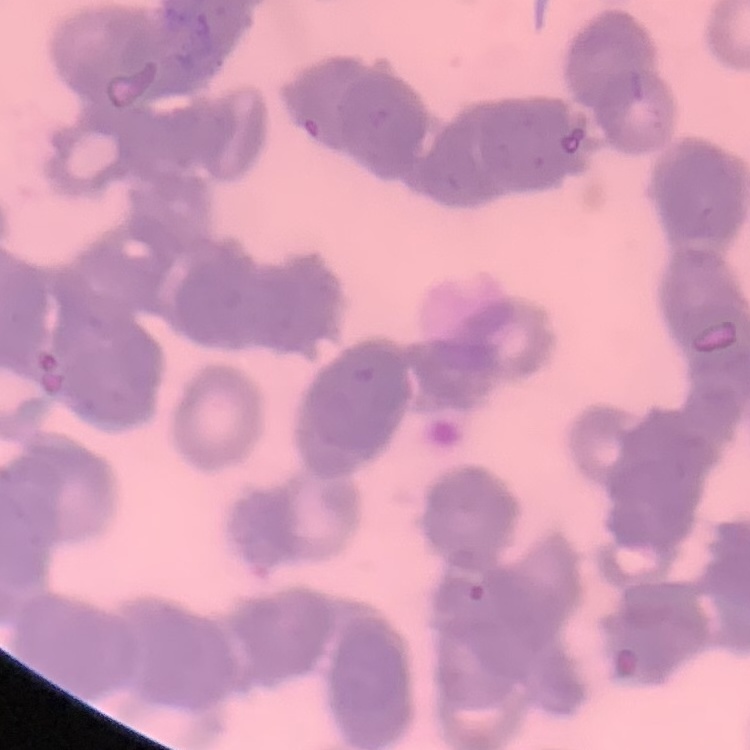
The red blood cells exhibit rouleaux formation. One tile cut from a larger photomicrograph. Thin blood smear. Stained with either Field's or Giemsa.